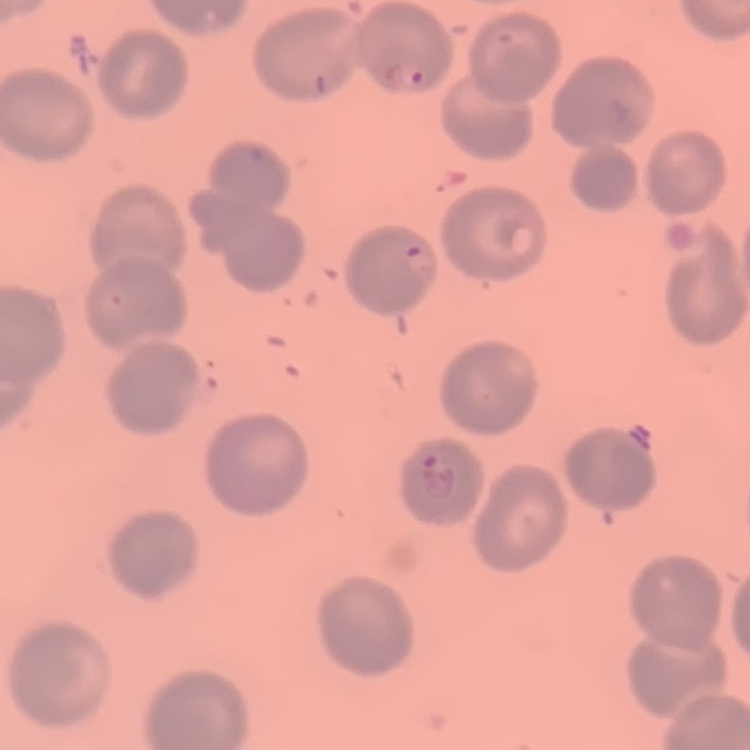
erythrocyte_morphology: no rouleaux formation
stain: Field's or Giemsa
preparation: thin blood film
image_type: square crop of a larger photomicrograph